Assess this cell for malaria.
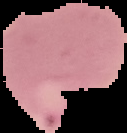

It is parasitized.

Summary:
  - Image type: segmented cell region with the area outside set to black
  - Preparation: thin blood smear
  - Image size: 127×133 pixels